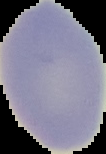

Summary:
  - Preparation: thin blood film
  - Malaria status: uninfected
  - Image size: 106×154 pixels
  - Image type: segmented cell region with the area outside set to black